Assess this cell for malaria.
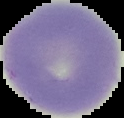
It is uninfected.

image size = 124×118 pixels
image type = segmented cell region with the area outside set to black
preparation = thin blood smear